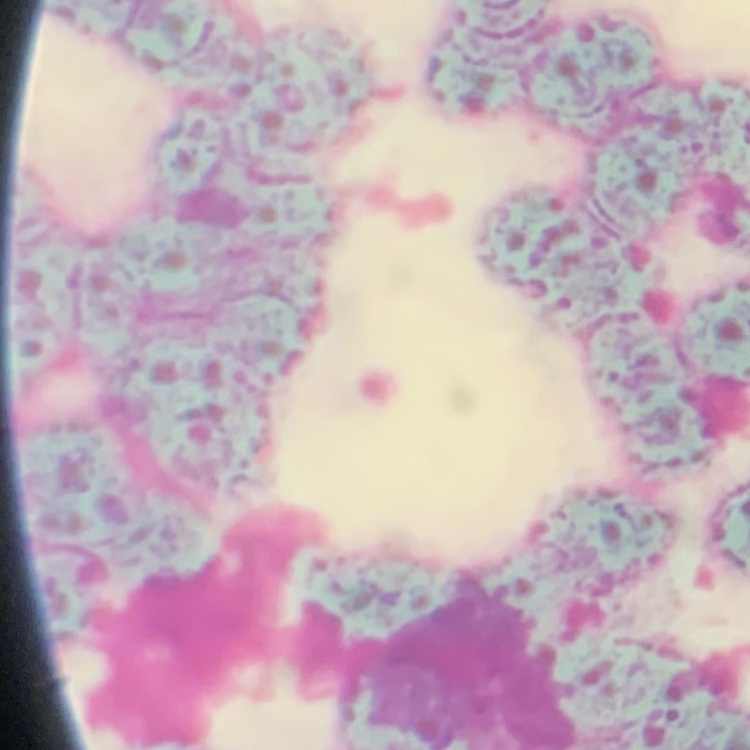
red blood cell morphology = rouleaux formation
image type = one tile cut from a larger photomicrograph
stain = Field's or Giemsa
preparation = thin peripheral smear